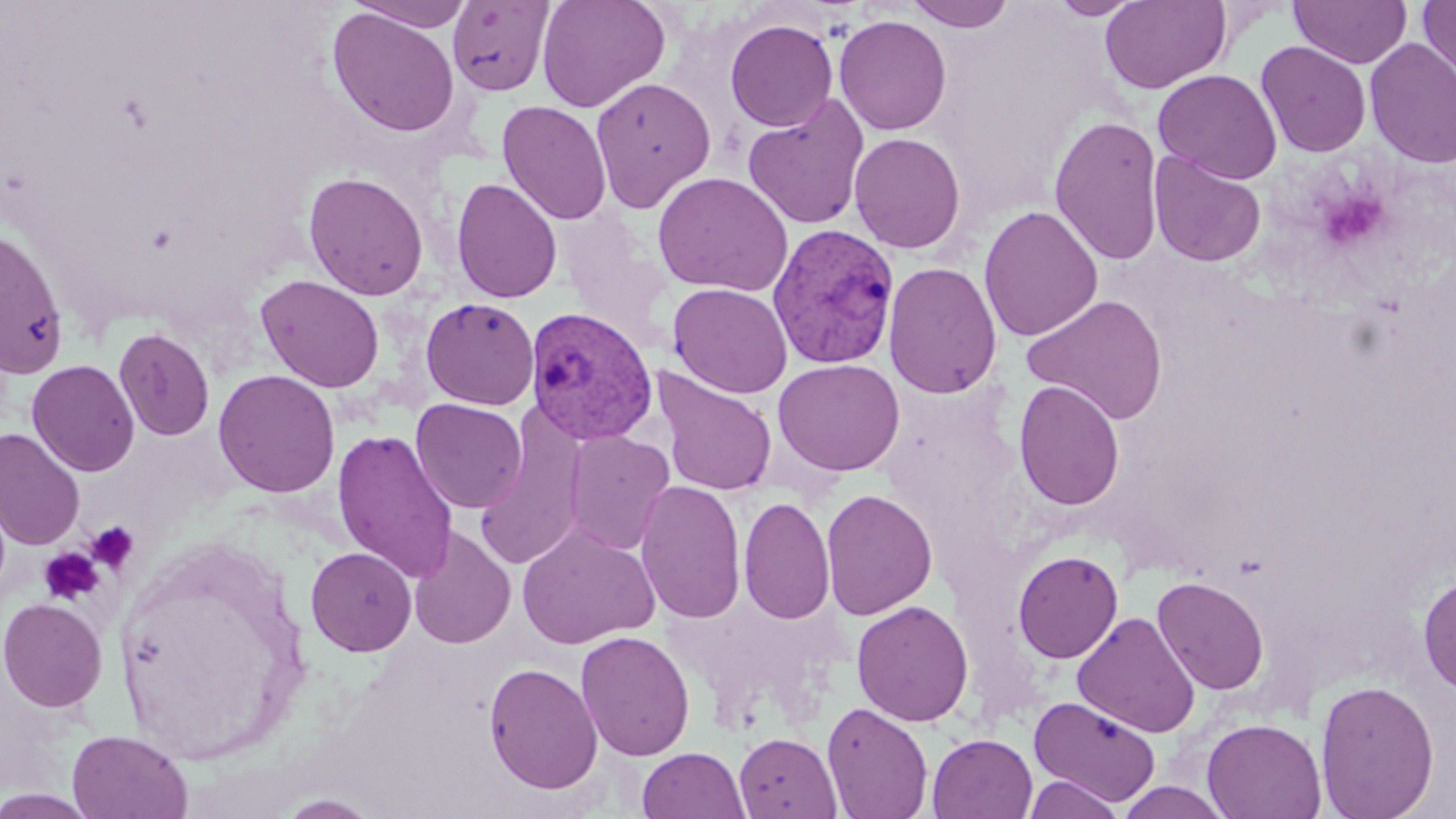

slide_level_diagnosis: Plasmodium vivax
preparation: thin blood film
magnification: 1000x
uninfected_red_blood_cell_locations: 'approximate bounding boxes as named x1/y1/x2/y2 corners in pixels: (x1=536, y1=0, x2=671, y2=113), (x1=905, y1=0, x2=1016, y2=32), (x1=1048, y1=0, x2=1145, y2=20), (x1=1289, y1=0, x2=1412, y2=68), (x1=1417, y1=0, x2=1456, y2=87), (x1=347, y1=1, x2=477, y2=31), (x1=447, y1=1, x2=555, y2=96), (x1=1099, y1=1, x2=1231, y2=93), (x1=326, y1=7, x2=461, y2=138), (x1=834, y1=14, x2=952, y2=136), (x1=724, y1=18, x2=838, y2=132), (x1=1364, y1=37, x2=1456, y2=168), (x1=1256, y1=41, x2=1371, y2=157), (x1=1153, y1=69, x2=1282, y2=183), (x1=590, y1=76, x2=716, y2=212), (x1=742, y1=93, x2=871, y2=230), (x1=496, y1=100, x2=612, y2=226), (x1=1049, y1=114, x2=1165, y2=266), (x1=848, y1=132, x2=966, y2=253), (x1=1149, y1=150, x2=1267, y2=267), (x1=652, y1=170, x2=794, y2=297), (x1=303, y1=171, x2=429, y2=300), (x1=451, y1=177, x2=563, y2=303), (x1=978, y1=205, x2=1104, y2=342), (x1=556, y1=208, x2=674, y2=340), (x1=1, y1=224, x2=70, y2=381), (x1=883, y1=262, x2=1002, y2=399), (x1=256, y1=274, x2=385, y2=393), (x1=667, y1=282, x2=793, y2=398), (x1=1021, y1=293, x2=1169, y2=425), (x1=421, y1=298, x2=539, y2=410), (x1=113, y1=327, x2=215, y2=441), (x1=772, y1=358, x2=906, y2=476), (x1=26, y1=359, x2=140, y2=477), (x1=652, y1=367, x2=778, y2=496), (x1=213, y1=369, x2=341, y2=498), (x1=1013, y1=379, x2=1125, y2=511), (x1=410, y1=398, x2=527, y2=513), (x1=474, y1=407, x2=590, y2=572), (x1=0, y1=427, x2=85, y2=550), (x1=332, y1=429, x2=459, y2=583), (x1=563, y1=430, x2=676, y2=555), (x1=635, y1=480, x2=747, y2=624), (x1=821, y1=488, x2=938, y2=620), (x1=739, y1=495, x2=835, y2=625), (x1=517, y1=522, x2=660, y2=649), (x1=407, y1=525, x2=515, y2=650), (x1=305, y1=546, x2=417, y2=656), (x1=1013, y1=550, x2=1124, y2=664), (x1=1417, y1=571, x2=1456, y2=695), (x1=1152, y1=575, x2=1270, y2=695), (x1=0, y1=597, x2=108, y2=712), (x1=851, y1=599, x2=974, y2=726), (x1=1072, y1=611, x2=1200, y2=738), (x1=575, y1=630, x2=695, y2=761), (x1=483, y1=661, x2=603, y2=794), (x1=1315, y1=679, x2=1440, y2=819), (x1=1028, y1=695, x2=1162, y2=808), (x1=823, y1=701, x2=933, y2=818), (x1=1202, y1=717, x2=1326, y2=818), (x1=67, y1=728, x2=194, y2=819), (x1=734, y1=732, x2=841, y2=818), (x1=927, y1=733, x2=1038, y2=819), (x1=637, y1=747, x2=750, y2=819), (x1=1023, y1=775, x2=1124, y2=819), (x1=1115, y1=781, x2=1232, y2=818), (x1=0, y1=789, x2=99, y2=818), (x1=271, y1=793, x2=386, y2=818)'
modality: light microscopy
stain: May-Grünwald-Giemsa
plasmodium_vivax_infected_red_blood_cell_locations: 'approximate bounding boxes as named x1/y1/x2/y2 corners in pixels: (x1=767, y1=222, x2=900, y2=369), (x1=525, y1=306, x2=660, y2=446)'
image_size: 1456×819 pixels
platelet_locations: 'approximate bounding boxes as named x1/y1/x2/y2 corners in pixels: (x1=1316, y1=189, x2=1390, y2=251), (x1=86, y1=520, x2=140, y2=574), (x1=39, y1=547, x2=105, y2=605)'
field_of_view: single